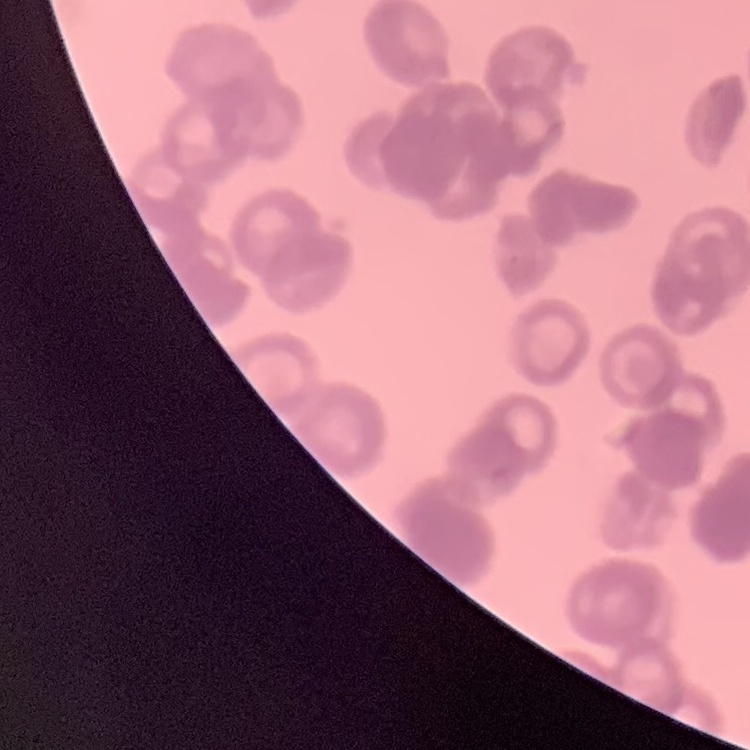

The erythrocytes show rouleaux formation. Thin blood smear. Field's or Giemsa stain. Square crop of a larger photomicrograph.